Comment on the morphology of the erythrocytes.
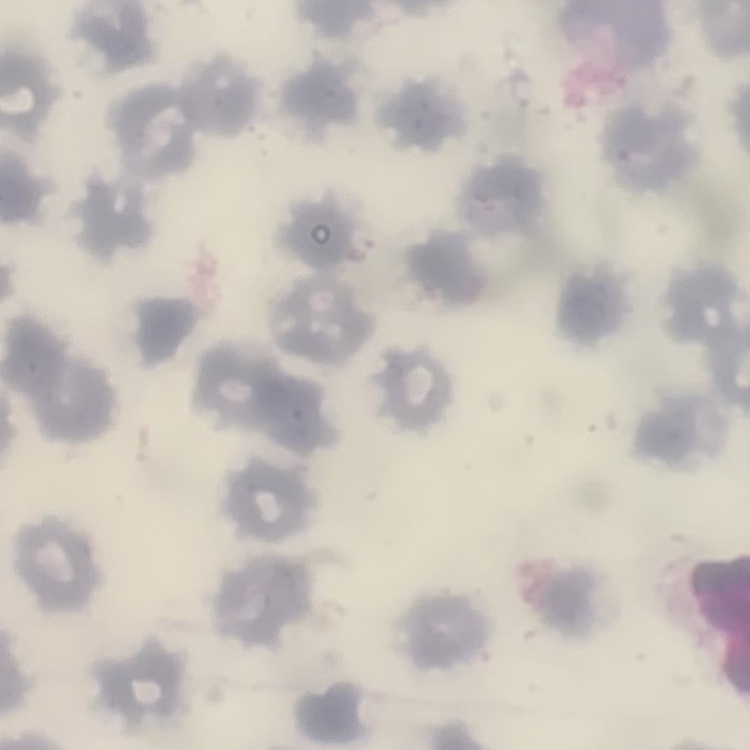

No rouleaux formation.

Summary:
  - Image type: one tile cut from a larger photomicrograph
  - Preparation: thin peripheral smear
  - Stain: Field's or Giemsa